Classify this cell by malaria status.
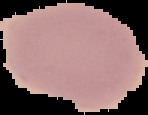

It is uninfected.

From a thin blood film. Image is 148×115 pixels. Cell region segmented out of the field of view; the surrounding area is masked to black.